Report the malaria status.
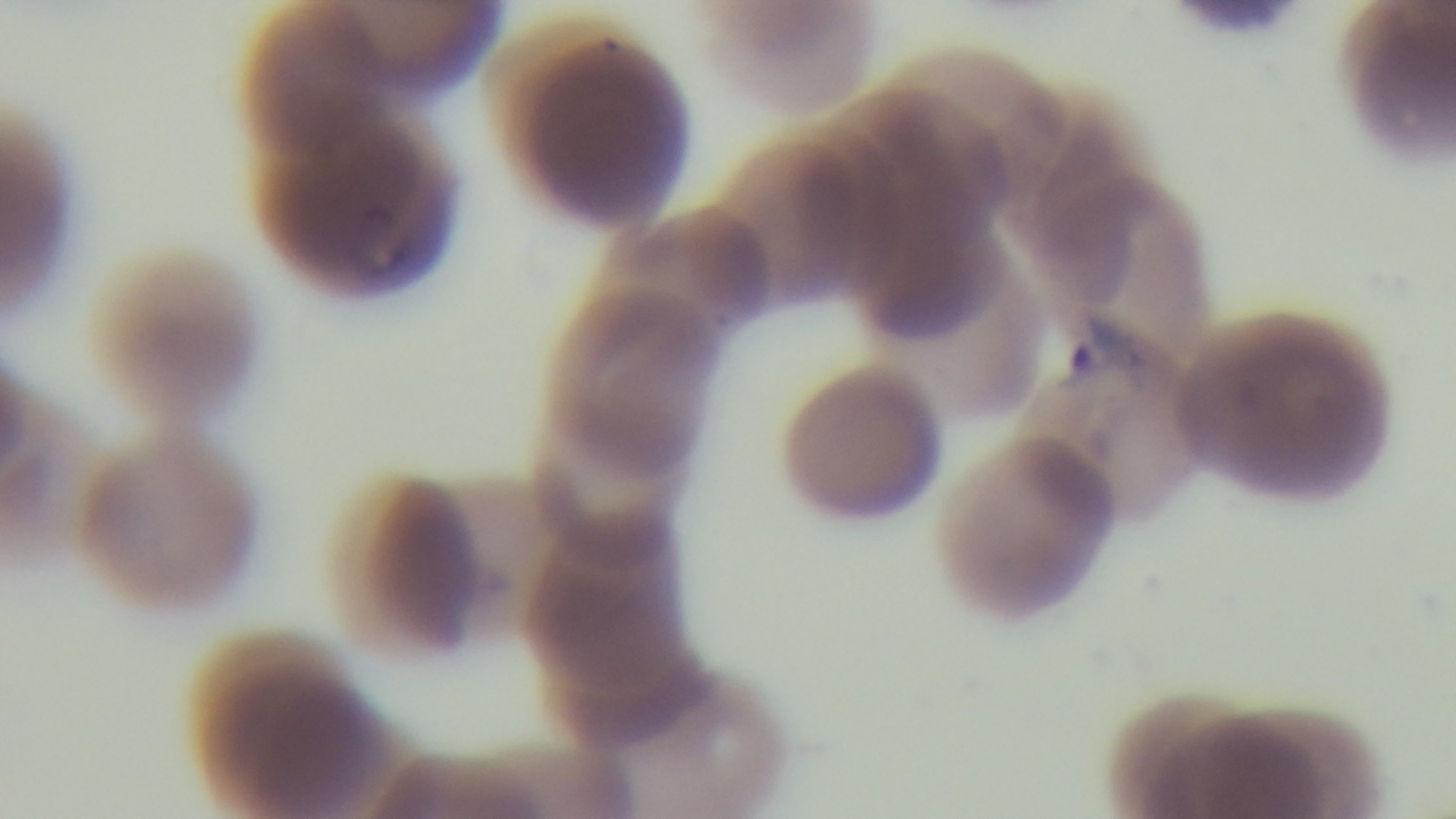
Positive.

Summary:
  - Field of view: single
  - Capture: mounted 4K digital camera
  - Preparation: thin
  - Modality: light microscopy
  - Stain: Giemsa
  - Objective: 100x oil immersion